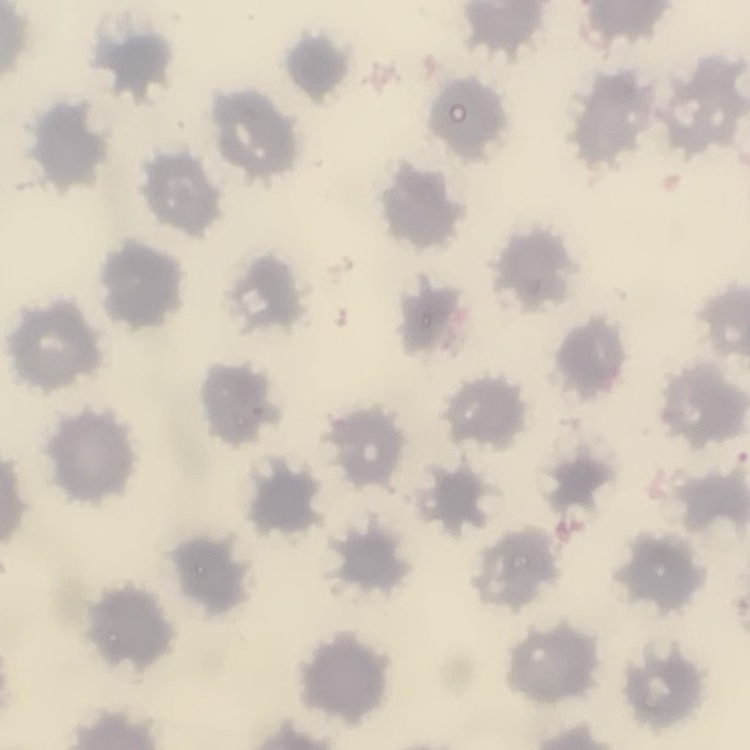

The red blood cells exhibit no rouleaux formation. Field's or Giemsa stain. Thin blood smear. One tile cut from a larger photomicrograph.